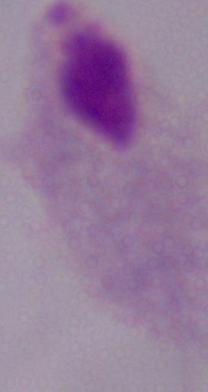
Summary:
  - Modality: micrograph
  - Identification: trichomonad
  - Magnification: 1000x